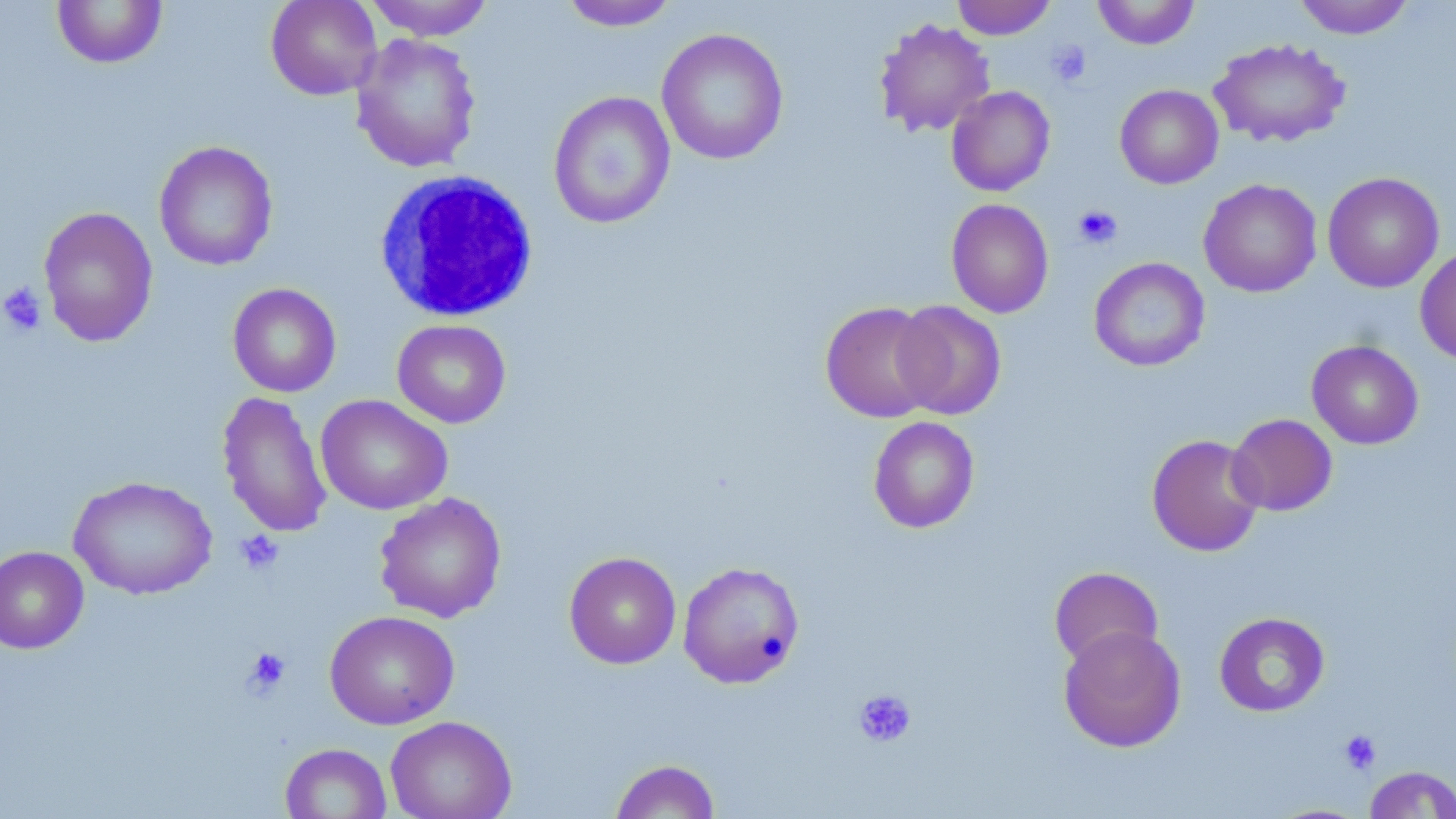 Approximate bounding boxes as (x1,y1)-(x2,y2) corner pairs in pixels. Platelet locations: (1046,40)-(1092,88), (1073,204)-(1122,250), (0,282)-(47,337), (235,530)-(285,575), (242,647)-(291,698), (852,689)-(916,747), (1338,730)-(1382,775). Uninfected red blood cell locations: (51,0)-(168,69), (265,0)-(382,100), (363,0)-(496,41), (952,0)-(1056,39), (1092,0)-(1200,49), (1293,0)-(1415,39), (559,1)-(680,31), (873,17)-(996,137), (656,28)-(789,165), (351,32)-(482,174), (1208,37)-(1351,148), (1115,84)-(1224,189), (946,86)-(1055,197), (548,90)-(676,229), (153,141)-(278,271), (1322,172)-(1444,293), (1198,178)-(1322,298), (946,198)-(1054,318), (37,206)-(159,347), (1415,246)-(1456,365), (1089,257)-(1210,372), (227,283)-(341,398), (892,300)-(1006,420), (820,301)-(941,423), (391,319)-(511,428), (1306,340)-(1423,449), (217,391)-(333,539), (315,395)-(453,515), (1226,413)-(1337,516), (868,416)-(979,533), (1146,433)-(1266,557), (68,476)-(217,600), (374,492)-(506,623), (0,546)-(89,654), (563,551)-(682,669), (677,560)-(804,688), (1049,566)-(1163,668), (324,610)-(460,730), (1214,612)-(1330,717), (1058,625)-(1187,753), (385,715)-(517,819), (280,743)-(391,818), (610,758)-(721,818), (1364,765)-(1456,818). White blood cell locations: (372,170)-(540,324). Slide-level diagnosis: negative for blood parasites. Thin blood smear. Captured at 1000x magnification. May-Grünwald-Giemsa stain. Single field of view. Optical microscopy. Image is 1456×819 pixels.